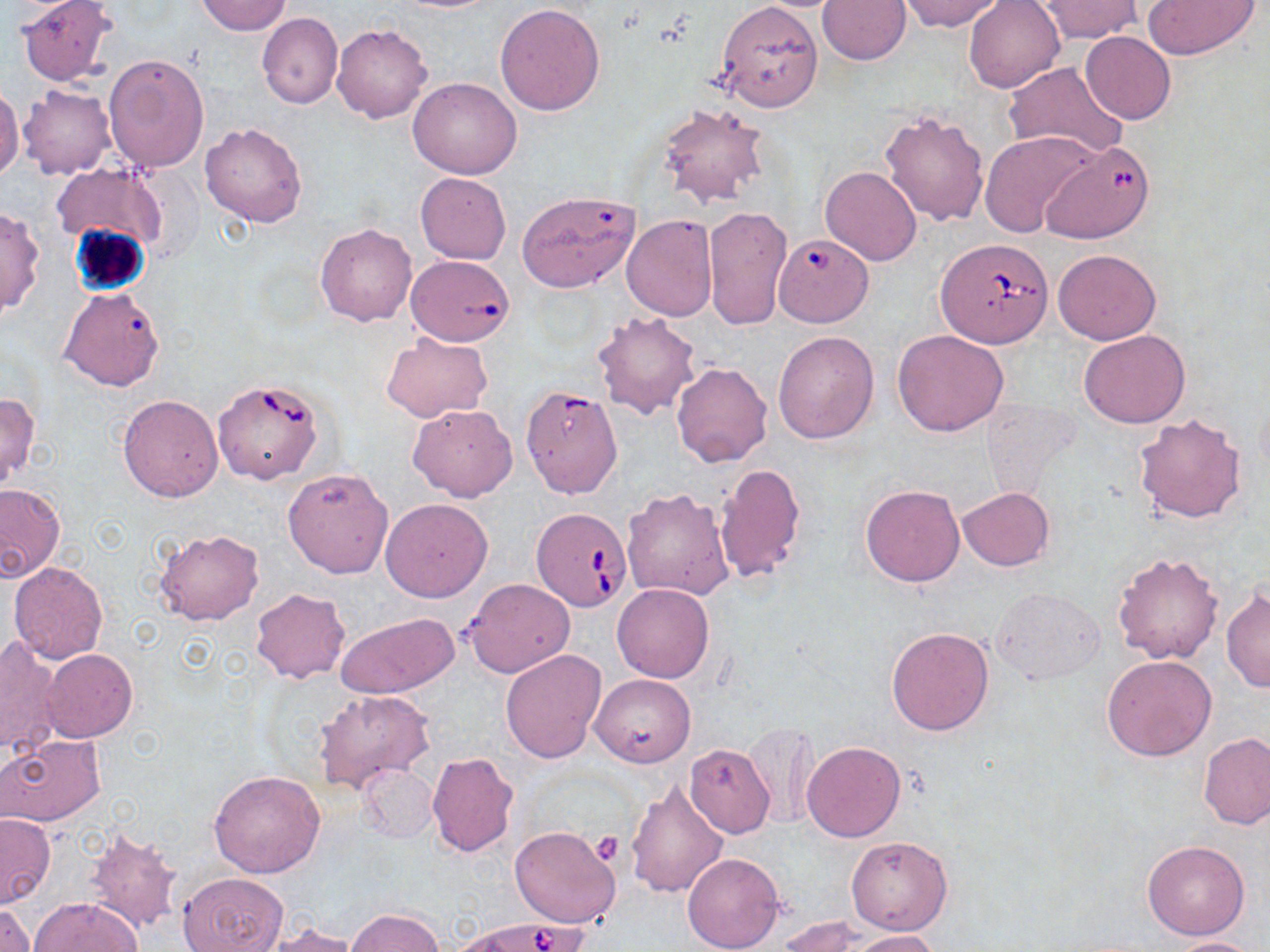
{
  "slide_level_diagnosis": "Babesia divergens",
  "stain": "May-Grünwald-Giemsa",
  "platelet_locations": "approximate bounding boxes as (x1,y1)-(x2,y2) corner pairs in pixels: (589,832)-(625,865)",
  "modality": "optical microscopy",
  "preparation": "thin blood smear",
  "image_size": "1270×952 pixels",
  "magnification": "1000x",
  "field_of_view": "one of a larger specimen",
  "uninfected_red_blood_cell_locations": "approximate bounding boxes as (x1,y1)-(x2,y2) corner pairs in pixels: (15,0)-(119,86), (388,0)-(504,13), (897,0)-(1005,33), (963,0)-(1065,93), (1142,0)-(1258,58), (195,1)-(291,35), (714,1)-(824,112), (818,1)-(910,65), (1035,2)-(1144,41), (494,3)-(605,115), (256,13)-(342,108), (332,23)-(433,124), (1080,31)-(1176,125), (103,54)-(209,174), (1004,62)-(1129,162), (408,76)-(521,179), (18,84)-(116,180), (0,85)-(22,182), (655,103)-(773,209), (879,109)-(990,227), (200,122)-(307,228), (980,131)-(1099,238), (51,163)-(166,253), (820,167)-(920,266), (415,173)-(511,264), (516,191)-(639,294), (0,206)-(42,319), (703,206)-(792,331), (622,215)-(718,320), (314,222)-(417,327), (1052,249)-(1161,345), (59,287)-(165,391), (592,309)-(703,421), (893,329)-(1010,438), (1079,329)-(1190,427), (772,330)-(878,444), (381,334)-(492,420), (672,362)-(772,468), (527,383)-(624,505), (0,389)-(42,491), (118,394)-(224,502), (408,404)-(517,501), (1134,413)-(1247,523), (715,462)-(808,584), (282,467)-(393,579), (0,482)-(64,581), (861,484)-(965,587), (622,486)-(734,600), (957,486)-(1054,572), (380,498)-(493,602), (154,528)-(264,626), (1111,552)-(1225,666), (8,562)-(108,665), (463,579)-(573,678), (612,583)-(714,682), (1221,586)-(1270,692), (992,587)-(1105,683), (250,588)-(350,682), (336,613)-(458,700), (886,627)-(994,735), (1,636)-(60,756), (39,648)-(138,743), (501,649)-(606,764), (1102,654)-(1216,761), (590,673)-(694,767), (313,689)-(434,792), (744,720)-(819,829), (0,733)-(108,827), (1200,734)-(1270,829), (801,741)-(905,842), (684,744)-(775,838), (427,751)-(518,857), (358,763)-(438,844), (208,770)-(325,877), (625,777)-(729,898), (0,813)-(55,907), (83,825)-(185,933), (509,825)-(621,929), (846,835)-(952,934), (1142,840)-(1249,939), (682,852)-(784,952), (180,873)-(285,952), (30,897)-(141,952), (1,901)-(36,952), (347,907)-(443,952), (778,916)-(871,950), (266,922)-(366,951), (849,930)-(942,951), (1164,937)-(1265,952)",
  "babesia_divergens_infected_red_blood_cell_locations": "approximate bounding boxes as (x1,y1)-(x2,y2) corner pairs in pixels: (1042,142)-(1155,242), (766,225)-(876,333), (938,239)-(1053,348), (406,254)-(515,367), (212,380)-(324,485), (531,508)-(632,611), (457,916)-(591,952)"
}